Describe the morphology of the red blood cells.
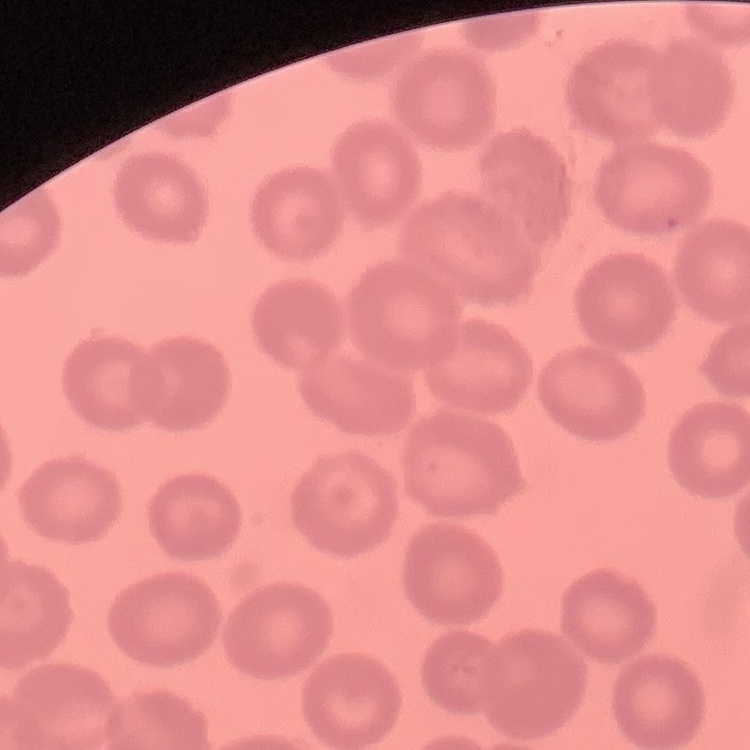
No rouleaux formation.

Summary:
  - Preparation: thin blood film
  - Stain: Field's or Giemsa
  - Image type: square crop of a larger photomicrograph